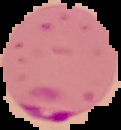
Cell region segmented out of the field of view; the surrounding area is masked to black. Malaria status: parasitized. From a thin blood smear. Image is 121×130 pixels.